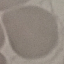 Malaria status: uninfected. Thin blood smear. Photographed with a smartphone camera at the microscope eyepiece. Automatically extracted cell patch, resized to 64 × 64 pixels. Giemsa-stained preparation.